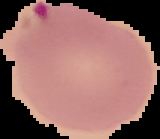
Summary:
  - Image size: 160×139 pixels
  - Preparation: thin blood film
  - Malaria status: parasitized
  - Image type: segmented cell region on a black background